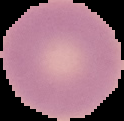 Image is 124×121 pixels. From a thin blood smear. Cell region segmented out of the field of view; the surrounding area is masked to black. Result: no Plasmodium parasites detected.